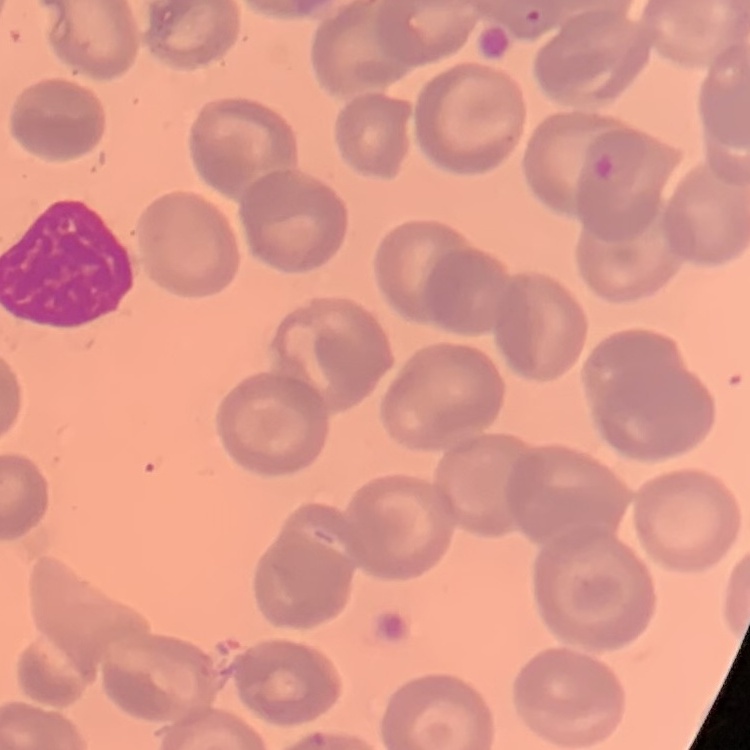 The red blood cells exhibit no rouleaux formation. Thin blood film. One tile cut from a larger photomicrograph. Stained with either Field's or Giemsa.